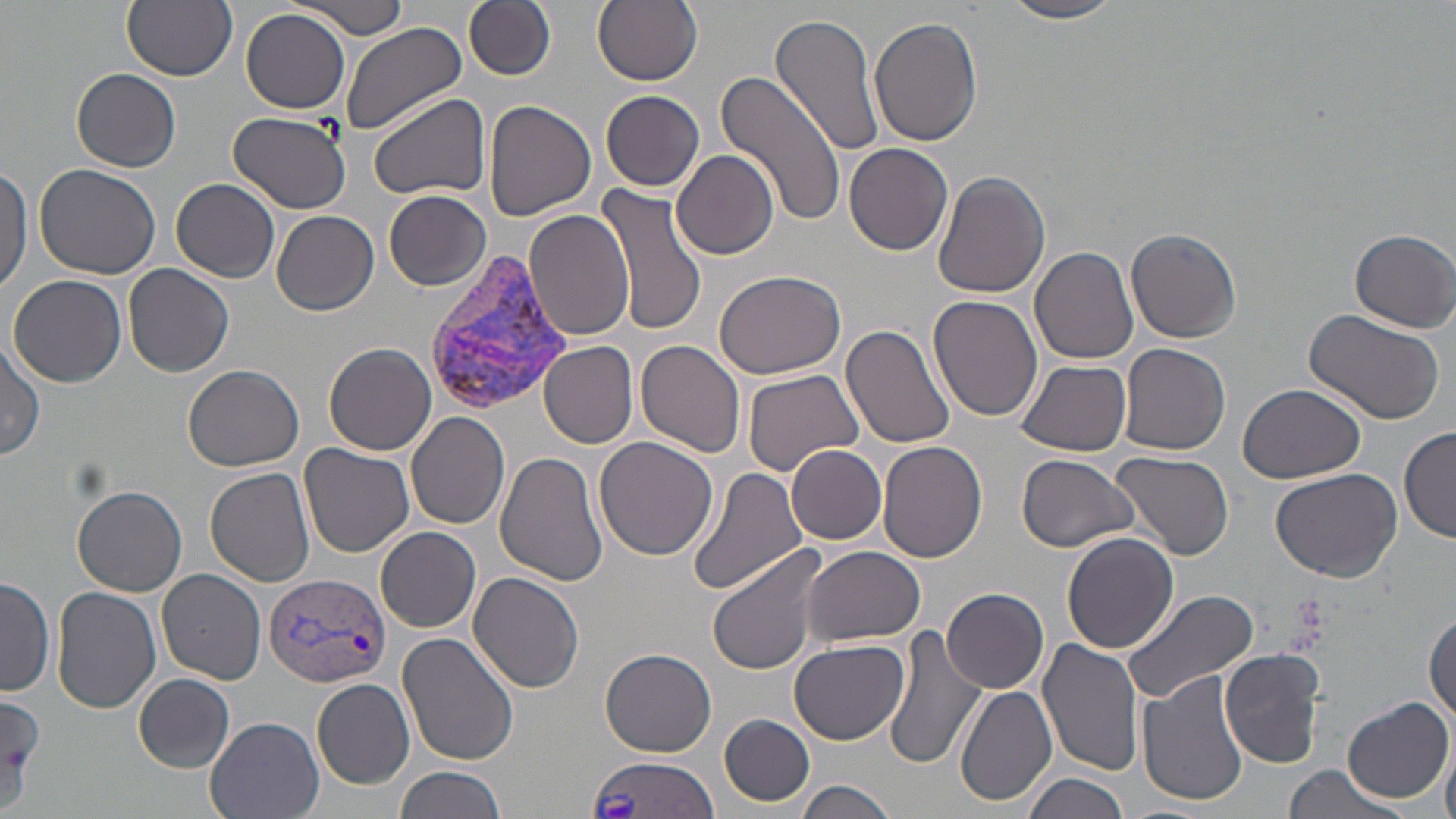

Summary:
  - Coordinate format: approximate bounding boxes as (x1, y1, x2, y2) in pixels
  - Plasmodium vivax-infected red blood cell locations: (422, 254, 566, 416), (263, 571, 391, 689), (581, 755, 722, 818)
  - Uninfected red blood cell locations: (121, 0, 236, 81), (464, 0, 555, 80), (593, 0, 702, 86), (289, 1, 411, 39), (1001, 1, 1127, 24), (241, 8, 350, 112), (772, 14, 885, 156), (869, 18, 983, 148), (338, 22, 466, 137), (716, 67, 846, 230), (73, 69, 182, 171), (601, 91, 704, 192), (369, 94, 490, 202), (483, 99, 596, 222), (228, 111, 351, 213), (845, 142, 954, 255), (673, 149, 779, 259), (34, 163, 162, 278), (1, 164, 32, 296), (932, 171, 1050, 299), (171, 177, 280, 282), (593, 181, 710, 338), (384, 190, 491, 291), (523, 208, 635, 340), (273, 211, 379, 316), (1126, 227, 1242, 344), (1350, 229, 1455, 332), (1030, 246, 1138, 365), (967, 250, 1101, 410), (123, 263, 235, 377), (712, 268, 845, 380), (8, 274, 127, 387), (929, 296, 1043, 423), (1304, 308, 1444, 423), (841, 321, 959, 449), (0, 339, 47, 461), (539, 340, 639, 450), (636, 340, 747, 457), (323, 342, 437, 456), (1119, 342, 1231, 456), (1017, 360, 1132, 457), (184, 364, 305, 471), (742, 368, 864, 475), (1238, 384, 1369, 485), (407, 412, 510, 529), (1399, 425, 1456, 543), (594, 437, 719, 560), (876, 442, 988, 564), (301, 443, 414, 557), (785, 445, 887, 544), (494, 451, 609, 586), (1110, 451, 1235, 562), (1017, 455, 1138, 552), (687, 467, 807, 597), (205, 468, 316, 587), (1270, 468, 1402, 583), (73, 485, 186, 596), (376, 527, 481, 632), (1062, 532, 1178, 655), (707, 545, 829, 674), (801, 547, 928, 647), (157, 568, 267, 684), (466, 572, 583, 694), (0, 577, 56, 698), (51, 587, 162, 714), (942, 587, 1048, 692), (1122, 588, 1259, 702), (1426, 612, 1456, 725), (883, 626, 987, 769), (398, 632, 519, 765), (1037, 635, 1142, 779), (790, 640, 910, 742), (599, 647, 717, 757), (1220, 649, 1327, 768), (1137, 669, 1249, 807), (134, 674, 234, 771), (311, 677, 415, 788), (954, 684, 1059, 807), (1341, 695, 1452, 804), (0, 696, 47, 802), (209, 701, 418, 803), (720, 714, 815, 807), (204, 715, 324, 819), (1442, 736, 1456, 819), (395, 765, 507, 819), (1279, 766, 1407, 819), (1024, 773, 1133, 819), (795, 780, 899, 819)
  - Platelet locations: (1287, 591, 1331, 641)
  - Slide-level diagnosis: Plasmodium vivax
  - Stain: May-Grünwald-Giemsa
  - Modality: optical microscopy
  - Magnification: 1000x
  - Image size: 1456×819 pixels
  - Field of view: single
  - Preparation: thin blood smear